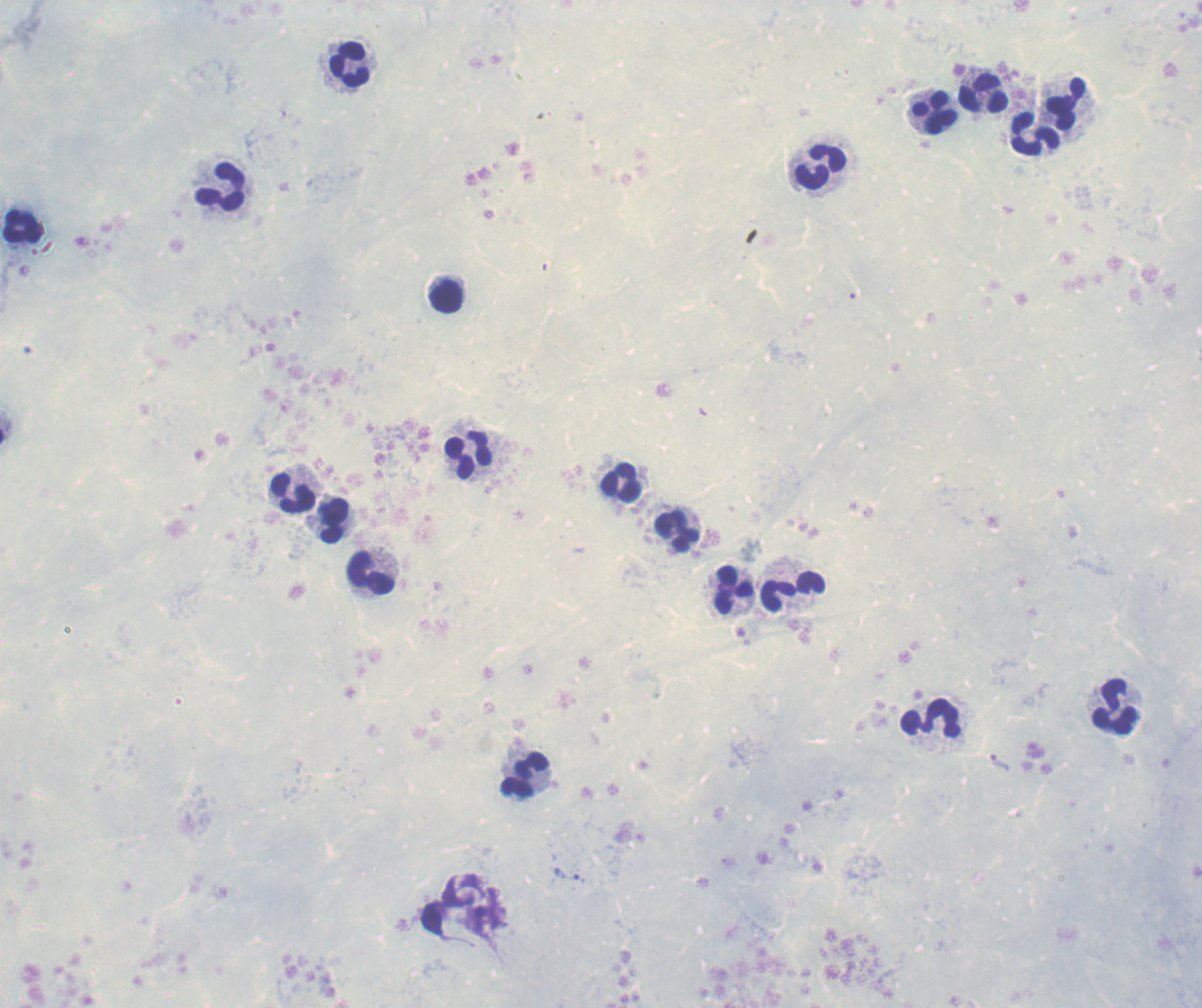
Approximate centers as [x, y] in pixels.
Summary:
  - Trophozoite locations: [567, 872]
  - Leukocyte locations: [349, 63], [984, 95], [1067, 104], [932, 114], [1035, 133], [819, 168], [221, 187], [22, 228], [447, 295], [469, 456], [620, 482], [293, 494], [336, 522], [677, 531], [372, 573], [811, 582], [734, 592], [779, 596], [1115, 707], [931, 719], [523, 775]
  - Magnification: 100x
  - Field of view: single
  - Image size: 1202×1008 pixels
  - Context: previously used in a real diagnosis
  - Preparation: thick blood smear
  - Stain: Romanowsky
  - Result: positive for Plasmodium parasites
  - Background quality: unsatisfactory